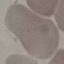

{
  "malaria_status": "uninfected",
  "image_type": "cell patch, automatically extracted from a larger field of view and resized to 64 × 64 pixels",
  "capture": "smartphone through the microscope eyepiece",
  "stain": "Giemsa",
  "preparation": "thin blood film"
}